Assess the morphology of the erythrocytes.
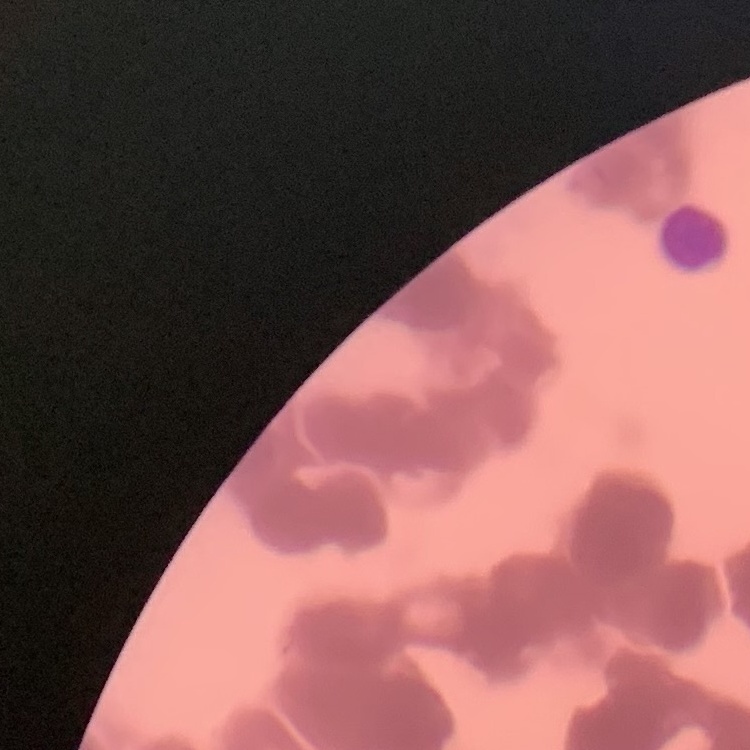

Rouleaux formation.

Summary:
  - Image type: square crop of a larger photomicrograph
  - Preparation: thin peripheral smear
  - Stain: Field's or Giemsa